Identify the blood parasite species.
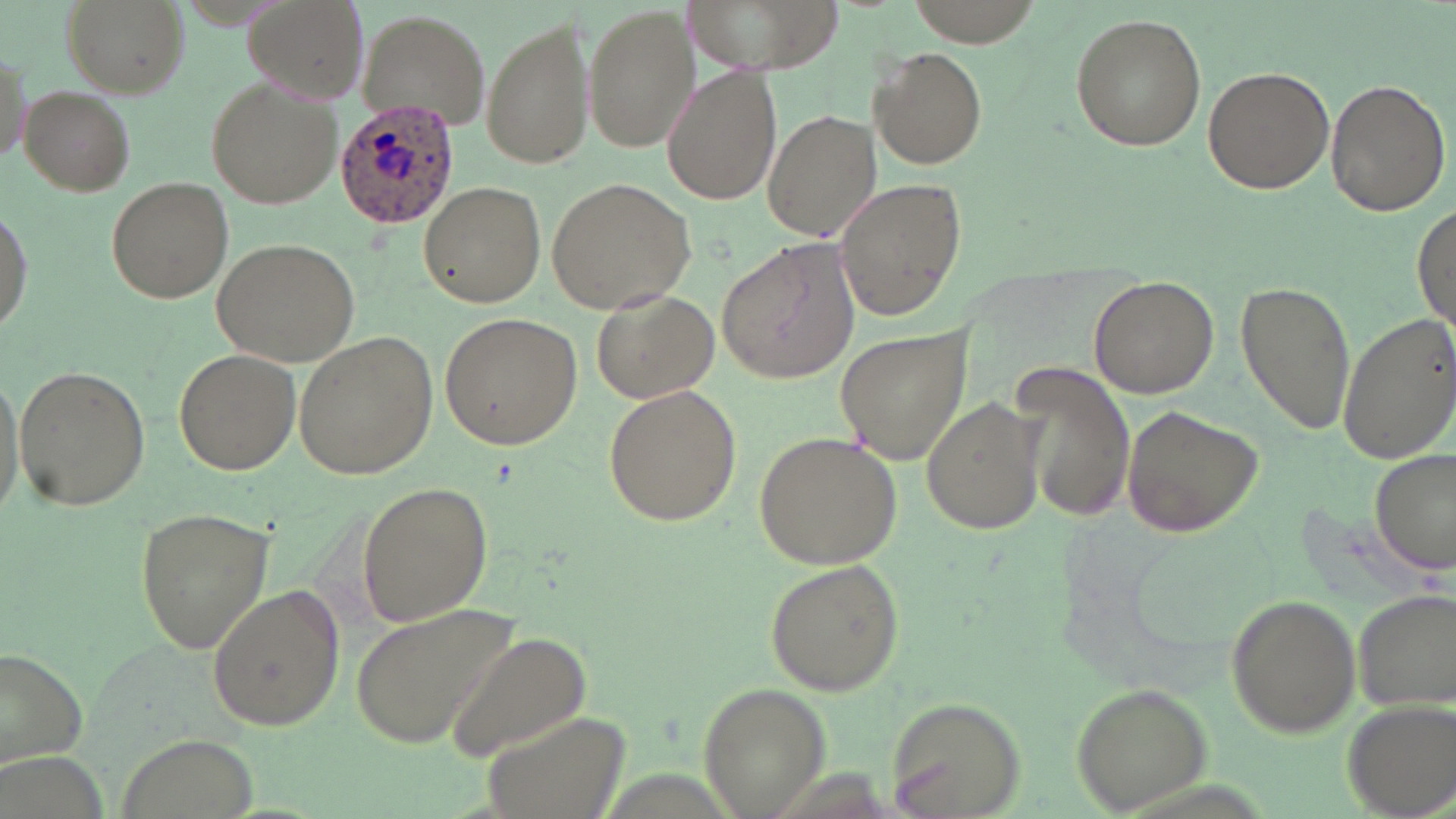

Plasmodium ovale.

Approximate bounding boxes as (x1, y1, x2, y2) in pixels. Uninfected red blood cell locations: (239, 0, 371, 108), (679, 0, 836, 77), (61, 1, 186, 99), (585, 4, 699, 154), (359, 10, 495, 133), (483, 13, 595, 169), (1070, 14, 1206, 152), (870, 47, 988, 171), (662, 64, 781, 207), (1201, 64, 1334, 195), (1325, 78, 1451, 218), (207, 80, 343, 207), (21, 86, 135, 196), (764, 109, 881, 244), (545, 175, 697, 316), (106, 176, 233, 302), (835, 176, 970, 324), (417, 182, 546, 306), (0, 201, 32, 340), (1412, 203, 1455, 339), (211, 238, 362, 367), (716, 242, 859, 383), (1088, 276, 1219, 397), (1234, 278, 1354, 438), (589, 289, 719, 404), (1335, 310, 1456, 467), (438, 312, 584, 449), (833, 322, 973, 468), (295, 330, 439, 479), (172, 347, 300, 475), (1010, 360, 1134, 524), (0, 362, 30, 528), (13, 366, 151, 511), (602, 386, 742, 526), (920, 396, 1046, 537), (1119, 403, 1263, 539), (755, 432, 900, 571), (1372, 448, 1453, 578), (357, 480, 494, 627), (133, 506, 275, 654), (763, 560, 904, 695), (206, 582, 345, 732), (1350, 587, 1455, 713), (1224, 594, 1361, 737), (349, 601, 525, 750), (446, 628, 593, 764), (0, 645, 89, 773), (697, 682, 833, 815), (1068, 682, 1214, 812), (885, 693, 1030, 818), (1342, 701, 1455, 817), (479, 708, 631, 819), (119, 734, 257, 819). Plasmodium ovale-infected red blood cell locations: (336, 101, 459, 229). May-Grünwald-Giemsa stain. Image is 1456×819 pixels. Single field of view. Thin blood film. Optical microscopy. 1000x magnification.